Identify the parasite.
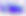

This is Toxoplasma gondii.

Micrograph. 400x magnification.